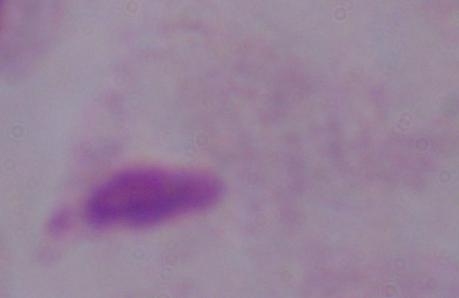
Micrograph. 1000x magnification. A trichomonad is shown.